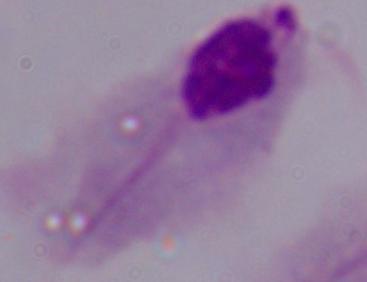
magnification: 1000x
identification: trichomonad
modality: micrograph